Describe the morphology of the red blood cells.
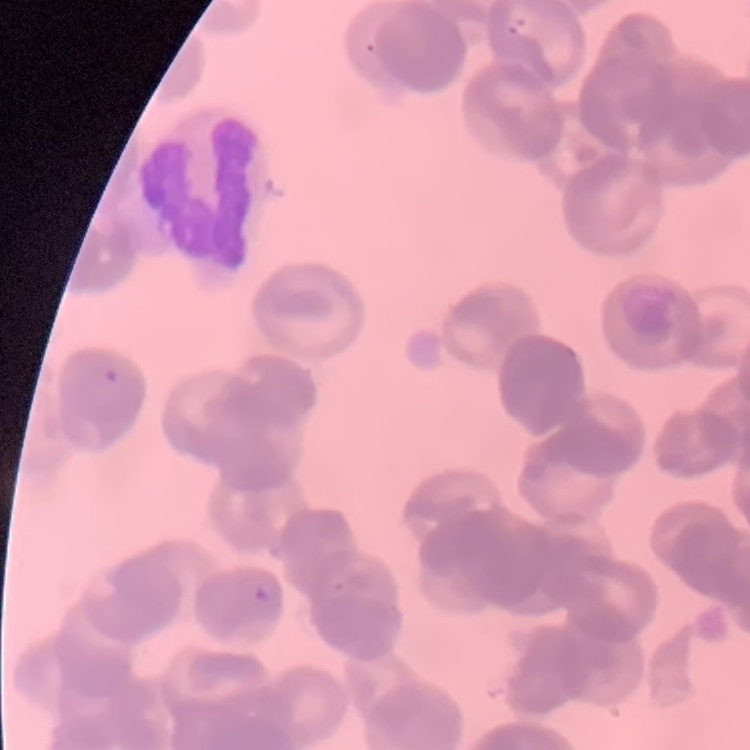
They show rouleaux formation.

Summary:
  - Preparation: thin blood film
  - Stain: Field's or Giemsa
  - Image type: square crop of a larger photomicrograph